Classify this cell by malaria status.
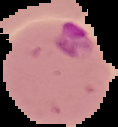

Parasitized.

Image is 118×127 pixels. From a thin blood smear. Segmented cell region on a black background.